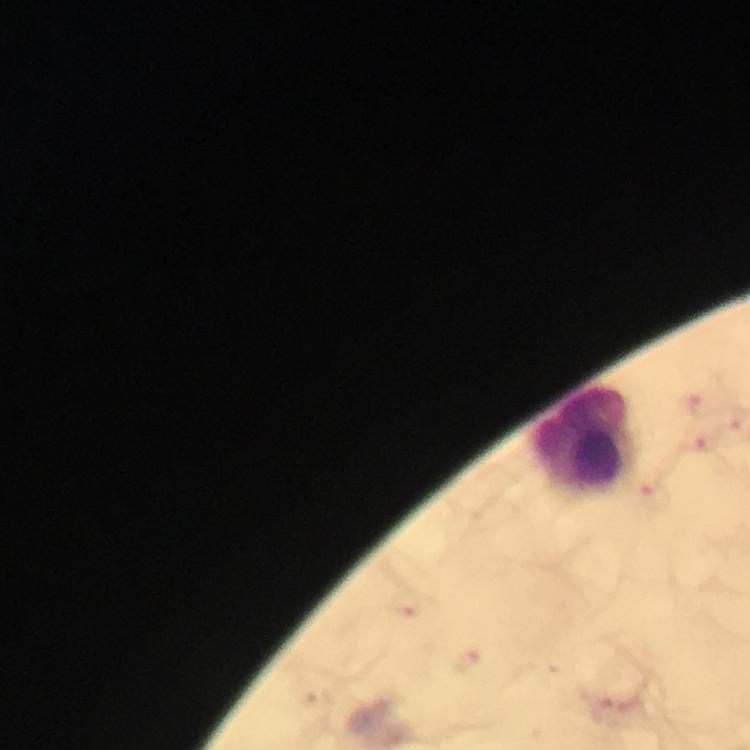 Approximate centers as (x, y) in pixels. Malaria parasite locations: (695, 396), (696, 445), (655, 494), (611, 710). Leukocyte locations: (584, 436). Photographed with a smartphone mounted on the microscope. 100x magnification. From a malaria diagnostic workup. Image is 750×750 pixels. A crop from one field of view. Immersion oil applied. Giemsa-stained preparation. Thick blood film.